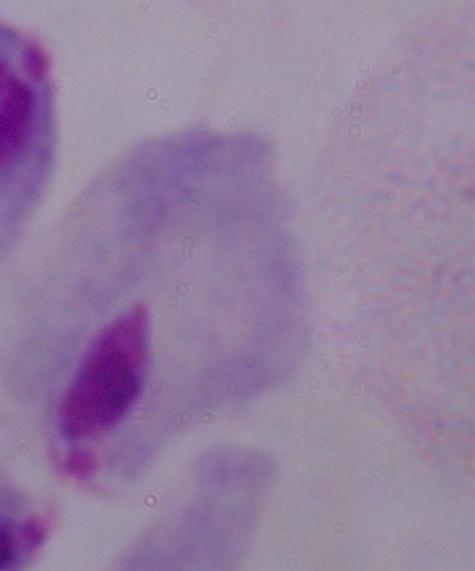

identification = trichomonad
magnification = 1000x
modality = photomicrograph